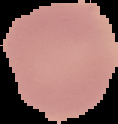
Summary:
  - Image size: 118×124 pixels
  - Image type: cell region segmented out of the field of view; surrounding area masked to black
  - Result: negative for Plasmodium parasites
  - Preparation: thin blood film